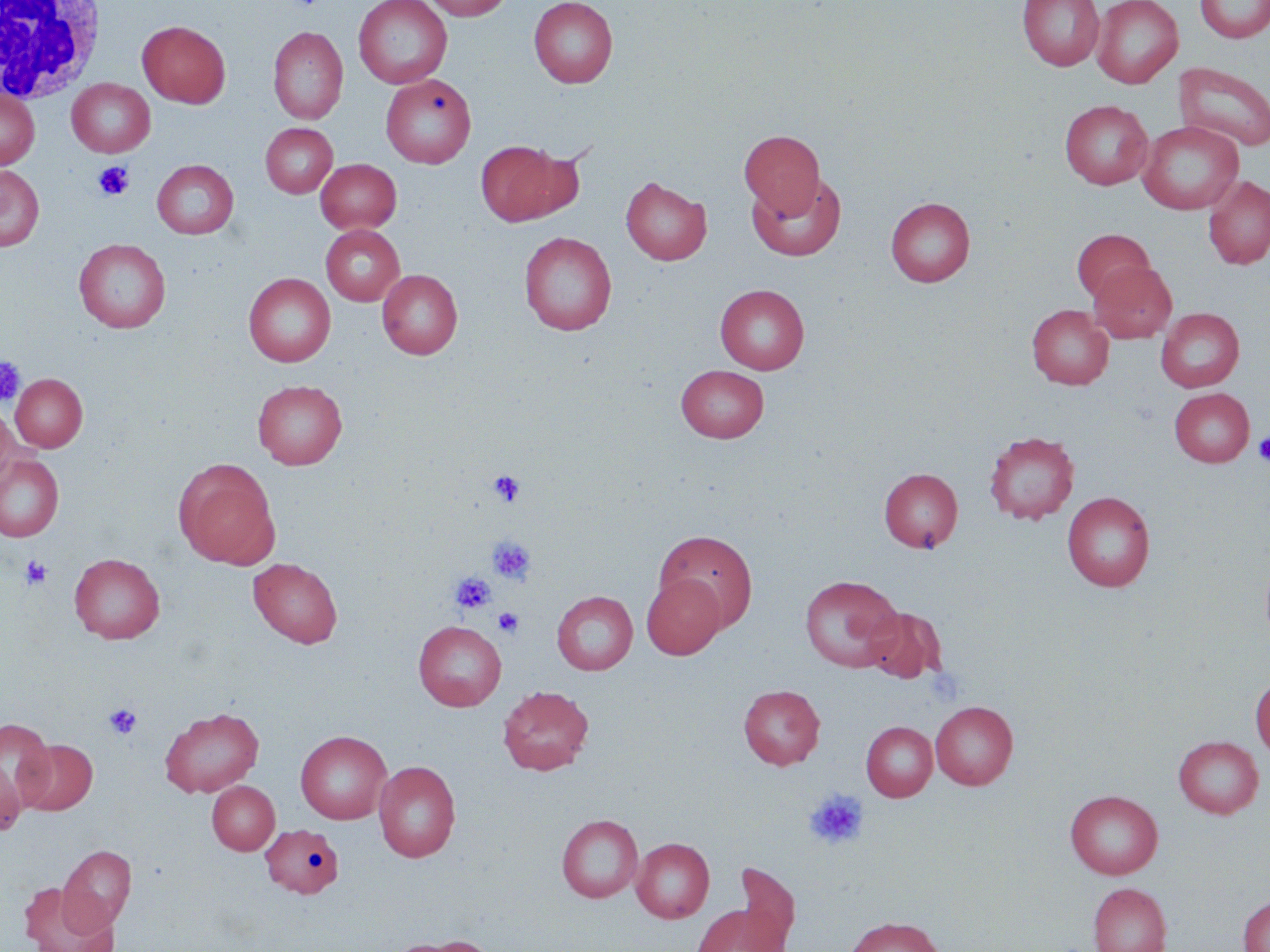 Approximate bounding boxes as (x1, y1, x2, y2) in pixels. White blood cell locations: (0, 2, 105, 104). Platelet locations: (93, 161, 134, 201), (0, 357, 26, 406), (1253, 431, 1270, 465), (487, 469, 526, 506), (488, 536, 536, 585), (20, 555, 52, 589), (451, 572, 496, 615), (493, 608, 524, 638), (104, 703, 142, 740), (804, 789, 868, 850). Uninfected red blood cell locations: (353, 0, 452, 88), (421, 0, 513, 20), (529, 0, 618, 88), (1017, 0, 1105, 70), (1091, 0, 1183, 88), (1195, 0, 1270, 43), (137, 20, 231, 108), (268, 26, 348, 124), (1175, 62, 1270, 152), (381, 74, 476, 168), (67, 78, 155, 157), (0, 90, 39, 169), (1059, 99, 1153, 189), (1137, 120, 1244, 214), (261, 123, 338, 198), (739, 130, 825, 217), (475, 139, 579, 226), (152, 159, 238, 239), (315, 159, 401, 233), (0, 164, 44, 251), (747, 172, 846, 262), (620, 176, 711, 264), (1202, 176, 1270, 269), (885, 197, 975, 286), (321, 224, 404, 305), (1071, 228, 1155, 304), (519, 231, 617, 335), (74, 238, 171, 333), (1087, 261, 1177, 343), (377, 269, 463, 359), (243, 272, 335, 367), (715, 284, 809, 374), (1027, 304, 1114, 389), (1156, 307, 1245, 392), (676, 364, 769, 443), (11, 374, 87, 451), (252, 379, 347, 469), (1169, 388, 1254, 466), (0, 402, 16, 487), (984, 431, 1080, 524), (0, 453, 64, 542), (174, 459, 280, 568), (879, 468, 963, 552), (1062, 491, 1155, 591), (653, 529, 759, 630), (69, 553, 165, 643), (248, 557, 343, 648), (641, 574, 726, 659), (800, 574, 903, 672), (551, 590, 638, 675), (863, 607, 946, 683), (413, 620, 507, 711), (1250, 675, 1270, 759), (738, 684, 824, 769), (497, 685, 594, 775), (931, 702, 1018, 789), (159, 706, 264, 797), (1, 719, 57, 814), (861, 721, 937, 801), (295, 730, 392, 824), (1173, 735, 1264, 818), (16, 739, 97, 815), (0, 756, 24, 837), (374, 760, 461, 862), (206, 781, 280, 855), (1066, 790, 1162, 879), (556, 814, 643, 903), (261, 824, 343, 897), (631, 837, 714, 922), (58, 845, 137, 932), (732, 863, 800, 950), (18, 881, 117, 952), (1088, 883, 1172, 952), (1238, 896, 1270, 952), (691, 904, 788, 952), (844, 916, 944, 952), (389, 936, 495, 952). Slide-level diagnosis: no evidence of blood parasites. Optical microscopy. 1000x magnification. Thin blood film. One field of a larger specimen. May-Grünwald-Giemsa-stained preparation. Image is 1270×952 pixels.